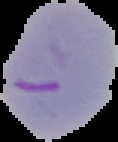 Cell region segmented out of the field of view; the surrounding area is masked to black. From a thin blood film. Image is 118×142 pixels. Result: malaria parasites detected.